Assess for malaria.
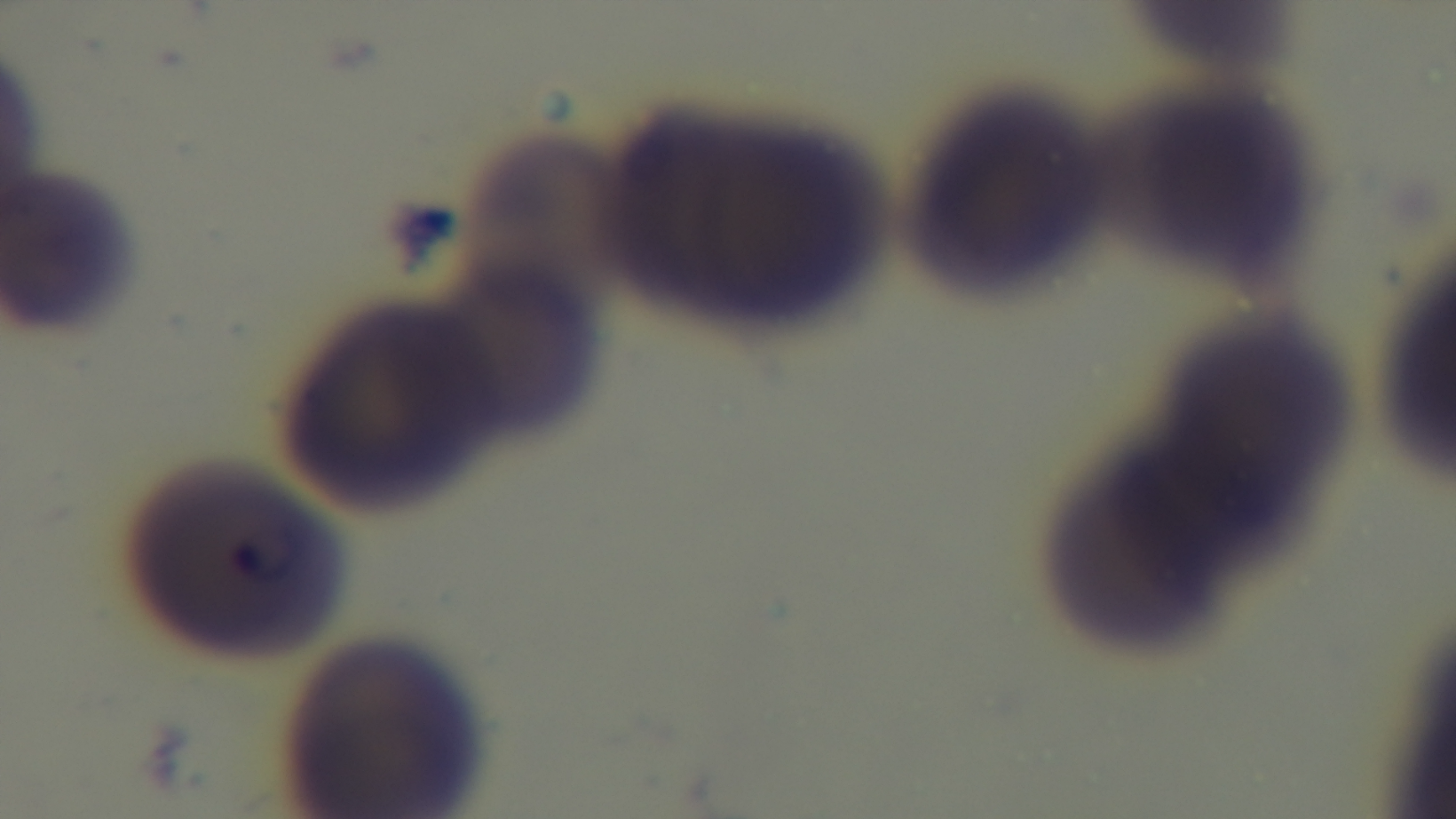

It is infected.

Summary:
  - Capture: mounted 4K digital camera
  - Objective: 100x oil immersion
  - Preparation: thin blood film
  - Field of view: one from the slide
  - Modality: light microscopy
  - Stain: Giemsa